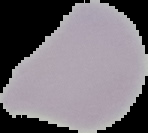

{
  "image_size": "148×133 pixels",
  "malaria_status": "uninfected",
  "preparation": "thin blood film",
  "image_type": "cell region segmented out of the field of view; surrounding area masked to black"
}